Locate every blood parasite and identify its species.
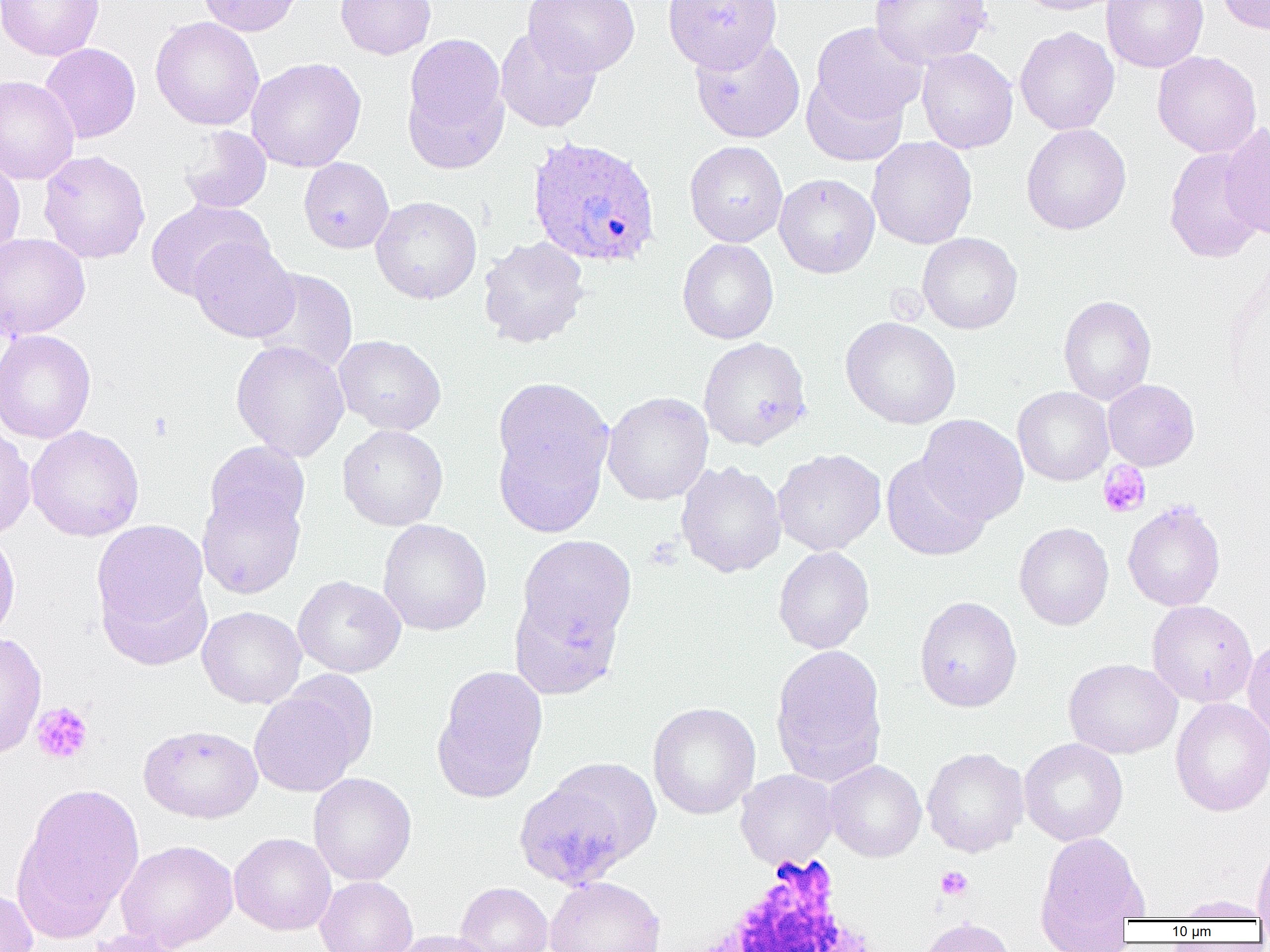
Approximate bounding boxes as [x1, y1, x2, y2] in pixels.
Plasmodium ovale-infected red blood cells: [526, 136, 661, 268].
No Plasmodium falciparum, Plasmodium malariae, Plasmodium vivax, Babesia divergens, or Trypanosoma brucei observed.

Platelet locations: [1098, 461, 1151, 518], [32, 702, 93, 764], [935, 866, 973, 900]. Uninfected red blood cell locations: [1, 0, 104, 61], [198, 0, 303, 36], [335, 0, 436, 60], [523, 0, 640, 77], [662, 0, 782, 72], [869, 0, 992, 67], [1019, 0, 1124, 15], [1101, 0, 1209, 73], [1216, 0, 1270, 35], [150, 17, 264, 130], [811, 22, 927, 125], [1015, 26, 1119, 135], [495, 27, 601, 133], [401, 33, 510, 172], [690, 35, 805, 143], [40, 43, 141, 143], [916, 47, 1018, 154], [1152, 51, 1262, 158], [246, 57, 366, 172], [801, 74, 909, 167], [0, 75, 80, 184], [1219, 122, 1270, 240], [1021, 124, 1131, 235], [178, 126, 272, 214], [867, 136, 977, 249], [685, 140, 788, 247], [1164, 148, 1267, 262], [39, 150, 151, 264], [0, 154, 25, 262], [299, 157, 394, 253], [774, 173, 880, 278], [370, 196, 482, 304], [145, 199, 270, 300], [0, 232, 90, 340], [917, 232, 1022, 334], [188, 236, 300, 342], [478, 236, 590, 348], [677, 238, 778, 344], [250, 267, 358, 376], [1058, 295, 1156, 405], [840, 317, 961, 429], [0, 330, 96, 444], [334, 335, 446, 435], [698, 337, 811, 450], [230, 340, 350, 462], [491, 378, 615, 535], [1103, 379, 1200, 470], [1013, 386, 1114, 486], [602, 392, 713, 505], [917, 414, 1028, 525], [0, 423, 36, 540], [25, 425, 145, 541], [337, 425, 448, 530], [205, 440, 310, 535], [772, 448, 886, 556], [881, 454, 991, 561], [676, 461, 786, 577], [197, 486, 305, 599], [1123, 500, 1225, 612], [91, 519, 210, 643], [378, 519, 492, 636], [1013, 521, 1114, 630], [0, 531, 20, 644], [515, 534, 637, 650], [773, 546, 874, 654], [99, 571, 212, 672], [293, 575, 406, 678], [509, 592, 625, 699], [914, 596, 1023, 712], [1147, 600, 1258, 707], [197, 606, 306, 709], [0, 633, 47, 759], [1243, 635, 1270, 742], [771, 645, 888, 785], [1064, 658, 1182, 759], [432, 665, 548, 803], [248, 681, 371, 798], [1169, 697, 1270, 817], [647, 701, 760, 820], [139, 724, 263, 823], [1019, 738, 1128, 846], [922, 747, 1029, 857], [824, 760, 926, 862], [512, 763, 657, 890], [735, 769, 837, 869], [308, 773, 416, 885], [12, 781, 145, 942], [229, 832, 336, 935], [1034, 832, 1150, 944], [115, 839, 238, 951], [1252, 843, 1270, 922], [315, 876, 418, 952], [544, 876, 666, 952], [455, 882, 553, 952], [0, 887, 38, 952], [1173, 895, 1269, 921], [919, 917, 1015, 952], [80, 928, 192, 952], [390, 930, 498, 952]. White blood cell locations: [677, 857, 893, 952]. Slide-level diagnosis: Plasmodium ovale. Captured at 1000x magnification. Optical microscopy. One field of a larger specimen. Image is 1270×952 pixels. Thin blood film.